Assess the morphology of the erythrocytes.
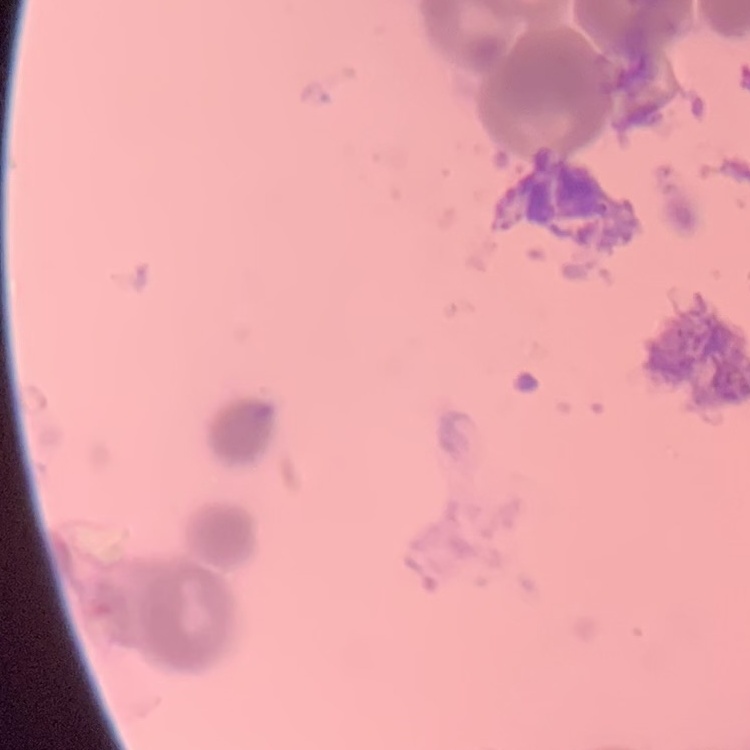
Rouleaux formation.

stain: Field's or Giemsa
image_type: square crop of a larger photomicrograph
preparation: thin peripheral smear